Assess this cell for malaria.
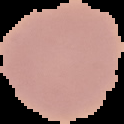
It is uninfected.

Image is 124×124 pixels. Cell region segmented out of the field of view; the surrounding area is masked to black. From a thin blood film.